Give the extent of all Plasmodium falciparum-infected red blood cells.
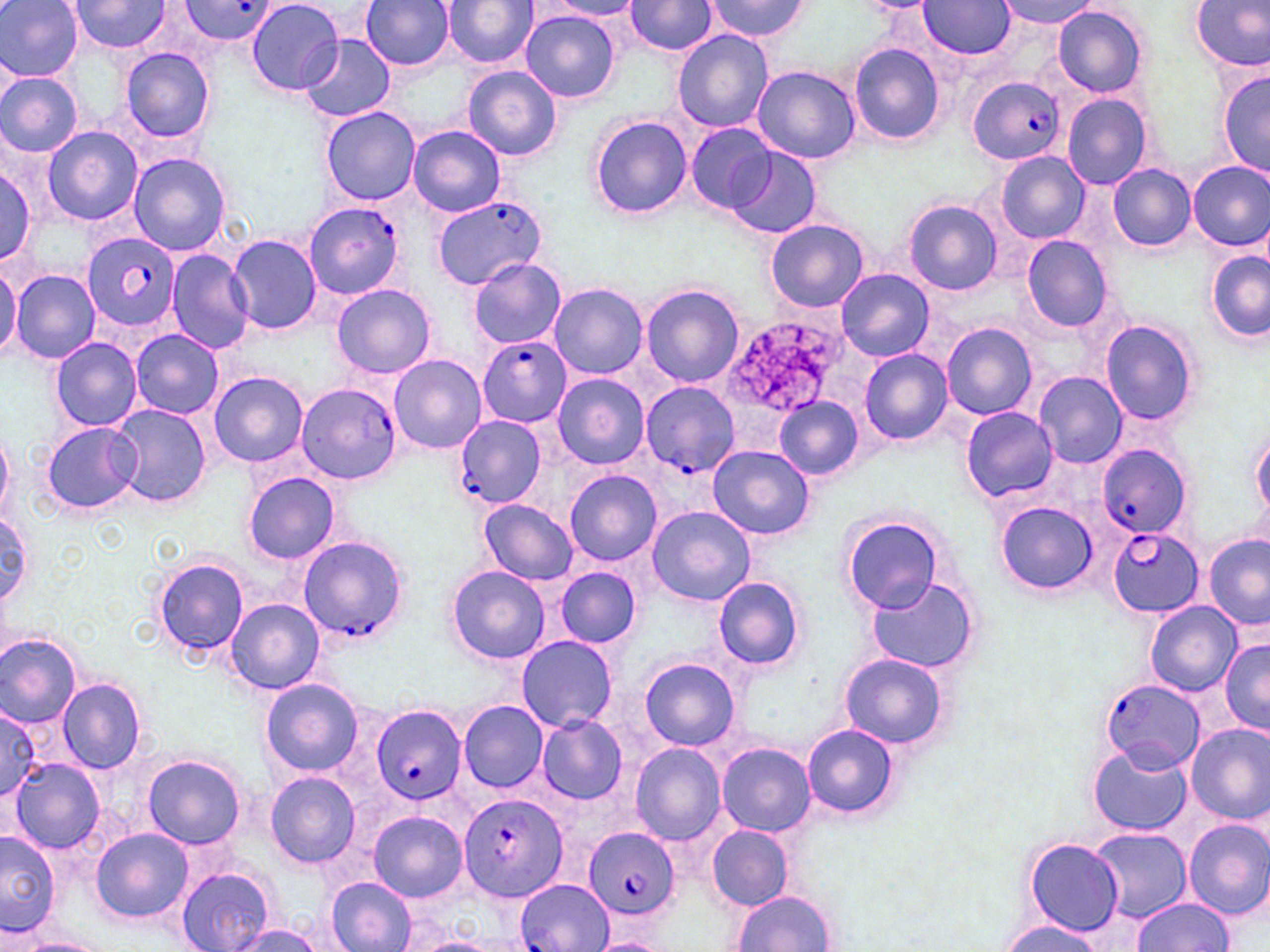
Approximate bounding boxes as named x1/y1/x2/y2 corners in pixels.
Plasmodium falciparum-infected red blood cells: (x1=182, y1=2, x2=279, y2=43), (x1=966, y1=76, x2=1064, y2=166), (x1=432, y1=195, x2=546, y2=291), (x1=306, y1=198, x2=407, y2=299), (x1=82, y1=232, x2=178, y2=333), (x1=478, y1=337, x2=570, y2=426), (x1=641, y1=380, x2=738, y2=477), (x1=297, y1=383, x2=401, y2=483), (x1=452, y1=414, x2=546, y2=511), (x1=1096, y1=444, x2=1192, y2=539), (x1=1108, y1=527, x2=1205, y2=616), (x1=297, y1=536, x2=409, y2=645), (x1=1098, y1=677, x2=1204, y2=773), (x1=370, y1=704, x2=467, y2=805), (x1=458, y1=793, x2=568, y2=903), (x1=583, y1=828, x2=681, y2=920), (x1=517, y1=879, x2=612, y2=952).

slide-level diagnosis = Plasmodium falciparum
modality = optical microscopy
field of view = one of a larger specimen
uninfected red blood cell locations = approximate bounding boxes as named x1/y1/x2/y2 corners in pixels: (x1=248, y1=0, x2=343, y2=95), (x1=362, y1=0, x2=455, y2=71), (x1=443, y1=0, x2=537, y2=67), (x1=703, y1=0, x2=806, y2=43), (x1=996, y1=0, x2=1100, y2=28), (x1=1, y1=1, x2=83, y2=81), (x1=68, y1=1, x2=170, y2=55), (x1=546, y1=1, x2=645, y2=19), (x1=625, y1=1, x2=717, y2=56), (x1=1190, y1=1, x2=1270, y2=72), (x1=919, y1=2, x2=1016, y2=59), (x1=1049, y1=5, x2=1149, y2=99), (x1=519, y1=10, x2=621, y2=104), (x1=672, y1=29, x2=774, y2=136), (x1=300, y1=34, x2=395, y2=122), (x1=847, y1=42, x2=945, y2=145), (x1=119, y1=46, x2=215, y2=143), (x1=751, y1=65, x2=860, y2=164), (x1=463, y1=66, x2=562, y2=161), (x1=1217, y1=69, x2=1269, y2=178), (x1=0, y1=71, x2=83, y2=157), (x1=7, y1=79, x2=112, y2=221), (x1=1061, y1=92, x2=1151, y2=190), (x1=321, y1=105, x2=421, y2=205), (x1=588, y1=114, x2=693, y2=220), (x1=686, y1=122, x2=776, y2=214), (x1=408, y1=126, x2=505, y2=217), (x1=42, y1=127, x2=142, y2=225), (x1=726, y1=147, x2=821, y2=239), (x1=127, y1=151, x2=232, y2=257), (x1=994, y1=151, x2=1090, y2=245), (x1=0, y1=158, x2=41, y2=264), (x1=1188, y1=161, x2=1270, y2=251), (x1=1107, y1=164, x2=1196, y2=250), (x1=903, y1=200, x2=1003, y2=296), (x1=766, y1=218, x2=869, y2=313), (x1=228, y1=235, x2=322, y2=333), (x1=1023, y1=236, x2=1113, y2=330), (x1=1206, y1=249, x2=1269, y2=342), (x1=166, y1=251, x2=253, y2=354), (x1=0, y1=258, x2=19, y2=361), (x1=469, y1=258, x2=567, y2=349), (x1=9, y1=267, x2=101, y2=365), (x1=836, y1=268, x2=933, y2=361), (x1=548, y1=282, x2=648, y2=379), (x1=331, y1=284, x2=436, y2=379), (x1=641, y1=284, x2=745, y2=389), (x1=1100, y1=320, x2=1200, y2=426), (x1=941, y1=322, x2=1038, y2=421), (x1=130, y1=329, x2=224, y2=418), (x1=51, y1=337, x2=143, y2=432), (x1=860, y1=349, x2=953, y2=446), (x1=389, y1=355, x2=485, y2=452), (x1=208, y1=372, x2=309, y2=467), (x1=1032, y1=372, x2=1127, y2=469), (x1=552, y1=374, x2=649, y2=469), (x1=775, y1=396, x2=862, y2=480), (x1=108, y1=403, x2=212, y2=509), (x1=962, y1=406, x2=1057, y2=502), (x1=41, y1=420, x2=138, y2=515), (x1=1251, y1=426, x2=1270, y2=520), (x1=0, y1=429, x2=13, y2=525), (x1=709, y1=445, x2=815, y2=540), (x1=566, y1=470, x2=662, y2=566), (x1=243, y1=472, x2=341, y2=564), (x1=478, y1=499, x2=579, y2=586), (x1=995, y1=501, x2=1099, y2=595), (x1=647, y1=506, x2=756, y2=606), (x1=1, y1=509, x2=35, y2=603), (x1=842, y1=518, x2=942, y2=615), (x1=1204, y1=534, x2=1270, y2=631), (x1=154, y1=558, x2=249, y2=660), (x1=447, y1=565, x2=550, y2=664), (x1=554, y1=568, x2=641, y2=647), (x1=866, y1=576, x2=981, y2=676), (x1=712, y1=577, x2=806, y2=672), (x1=225, y1=598, x2=325, y2=695), (x1=1146, y1=602, x2=1240, y2=695), (x1=0, y1=635, x2=81, y2=728), (x1=516, y1=636, x2=618, y2=731), (x1=1218, y1=637, x2=1268, y2=737), (x1=838, y1=652, x2=951, y2=751), (x1=639, y1=656, x2=741, y2=752), (x1=261, y1=678, x2=363, y2=777), (x1=57, y1=679, x2=146, y2=773), (x1=458, y1=700, x2=547, y2=793), (x1=0, y1=707, x2=44, y2=798), (x1=535, y1=714, x2=628, y2=805), (x1=801, y1=722, x2=900, y2=819), (x1=1186, y1=723, x2=1270, y2=824), (x1=716, y1=742, x2=816, y2=836), (x1=630, y1=743, x2=724, y2=846), (x1=1088, y1=743, x2=1192, y2=836), (x1=142, y1=755, x2=247, y2=849), (x1=10, y1=757, x2=106, y2=854), (x1=264, y1=772, x2=360, y2=868), (x1=369, y1=811, x2=468, y2=902), (x1=1183, y1=817, x2=1270, y2=920), (x1=706, y1=824, x2=795, y2=910), (x1=92, y1=828, x2=193, y2=922), (x1=1090, y1=828, x2=1191, y2=921), (x1=0, y1=830, x2=59, y2=935), (x1=1022, y1=837, x2=1123, y2=936), (x1=176, y1=864, x2=276, y2=952), (x1=326, y1=877, x2=418, y2=952), (x1=730, y1=890, x2=838, y2=952), (x1=1132, y1=897, x2=1233, y2=951), (x1=999, y1=920, x2=1108, y2=951), (x1=225, y1=925, x2=329, y2=951), (x1=8, y1=935, x2=108, y2=952), (x1=405, y1=935, x2=503, y2=952)
preparation = thin blood film
magnification = 1000x
image size = 1270×952 pixels
stain = May-Grünwald-Giemsa